Identify the preparation type.
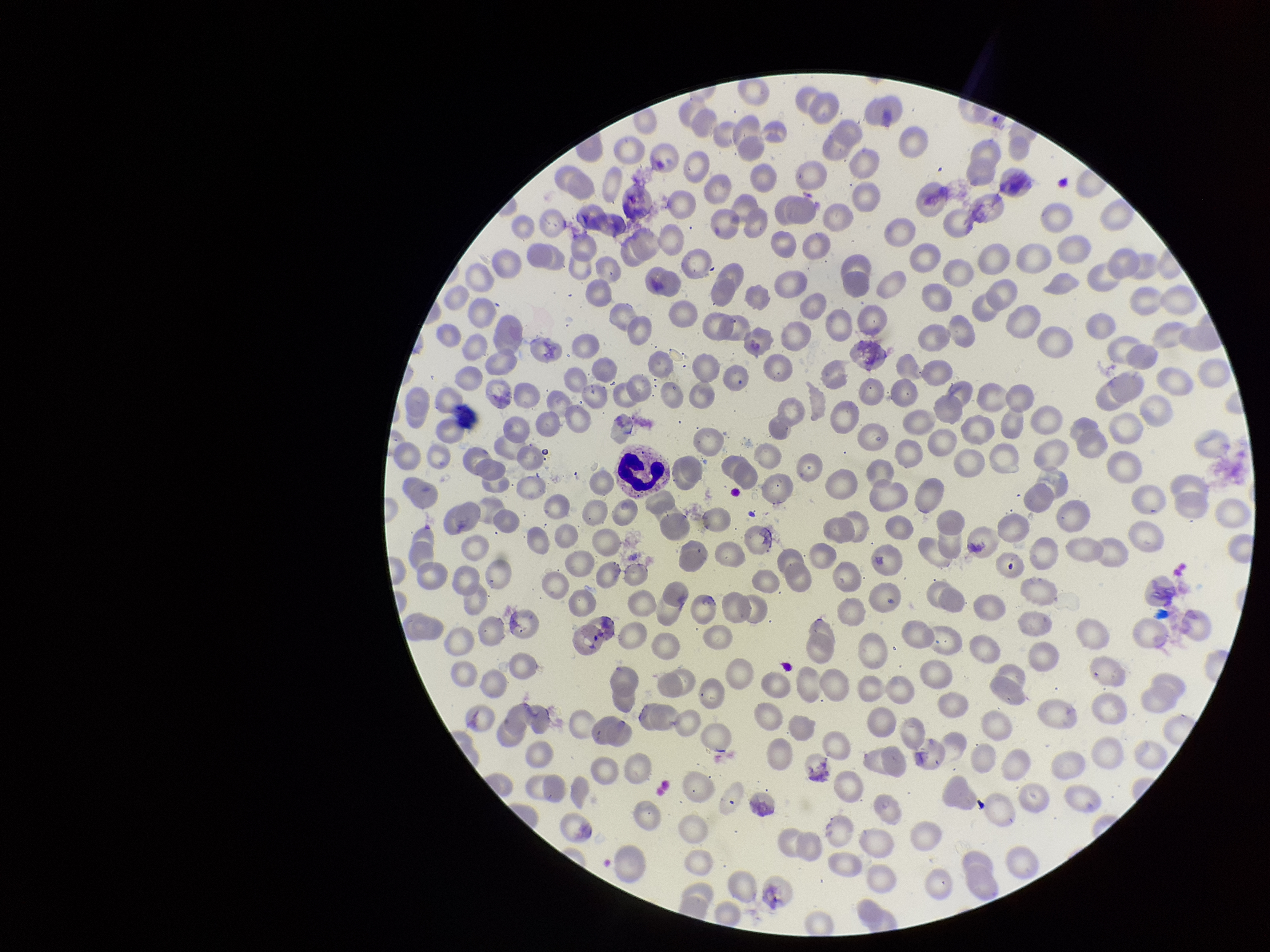
Thin.

Summary:
  - Patient malaria status: infected
  - Field of view: one from this slide
  - Capture: smartphone photograph through the microscope eyepiece
  - Red blood cell count: 262
  - Image size: 1270×952 pixels
  - Parasitized red blood cell count: 0
  - Species reported for this patient: Plasmodium vivax
  - Parasitized red blood cells: none identified
  - Stain: Giemsa